Report the malaria status of this cell.
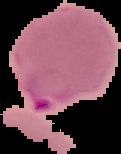
Parasitized.

preparation = thin blood smear
image size = 121×154 pixels
image type = cell region segmented out of the field of view; surrounding area masked to black